Outline every parasitised red blood cell, every trophozoite, every gametocyte, every leukocyte, and every artifact (platelet-like body, stain precipitate, or debris).
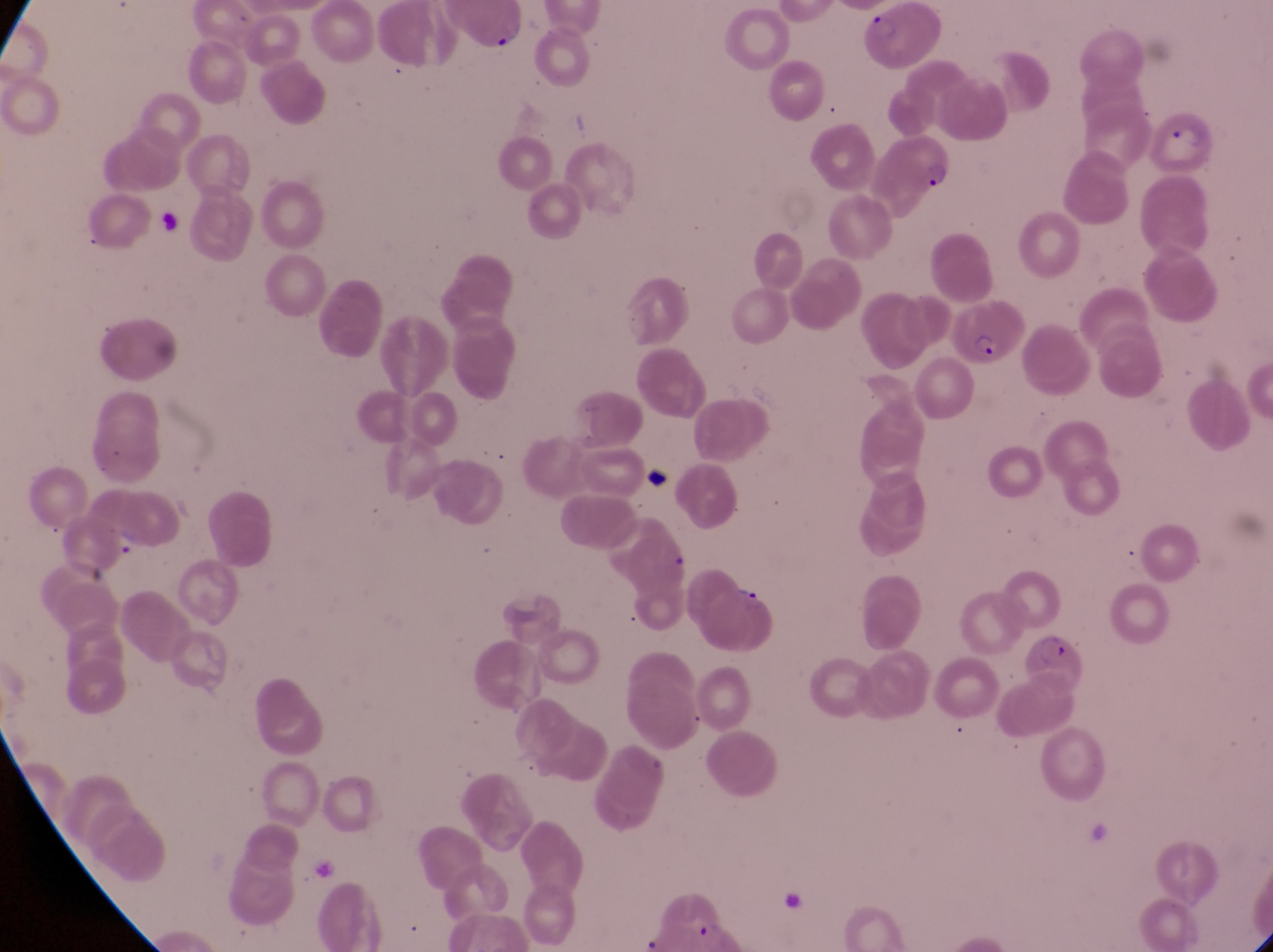
Approximate bounding boxes as left top right bottom in pixels.
Parasitised red blood cells: 863 5 948 75; 1133 102 1216 180; 871 132 956 222; 949 300 1018 367; 701 579 784 661; 1025 631 1097 711.
No leukocytes observed.
Artifacts (platelet-like body, stain precipitate, or debris): 486 27 525 55; 152 212 195 251; 634 462 684 497.

capture: smartphone photograph through the eyepiece of an Olympus CX-23 microscope
preparation: thin blood film
country: Uganda
image_size: 1273×952 pixels
magnification: 1000x
field_of_view: single